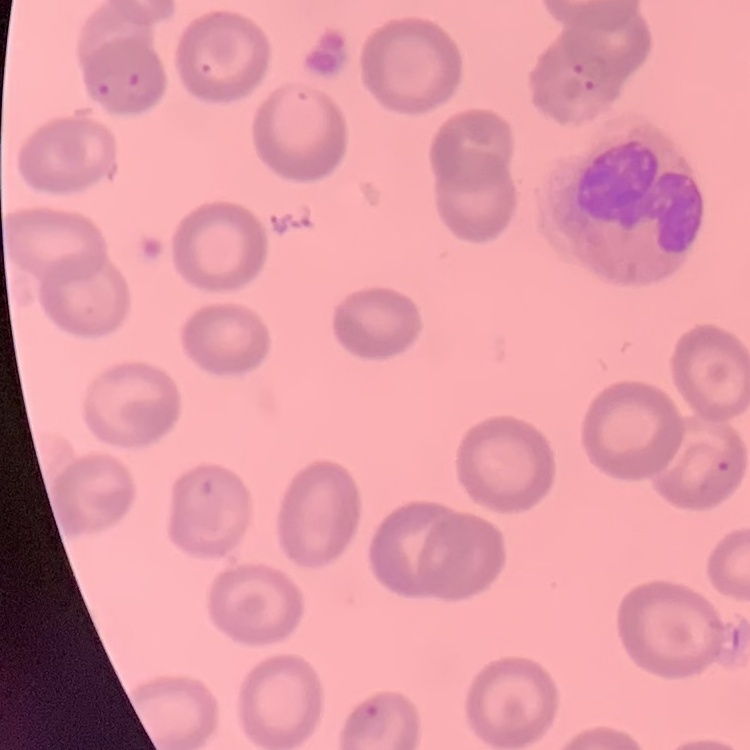
{
  "erythrocyte_morphology": "no rouleaux formation",
  "stain": "Field's or Giemsa",
  "image_type": "one tile cut from a larger photomicrograph",
  "preparation": "thin blood film"
}